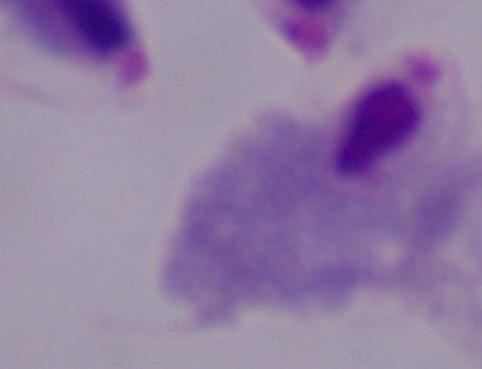
modality = photomicrograph
magnification = 1000x
identification = trichomonad